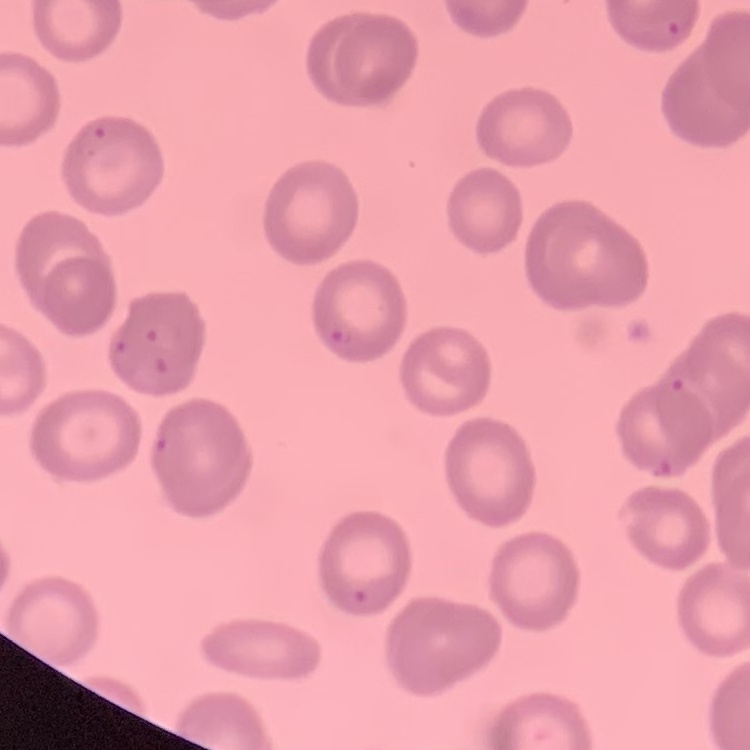

The erythrocytes exhibit no rouleaux formation. Thin peripheral smear. Field's or Giemsa stain. One tile cut from a larger photomicrograph.